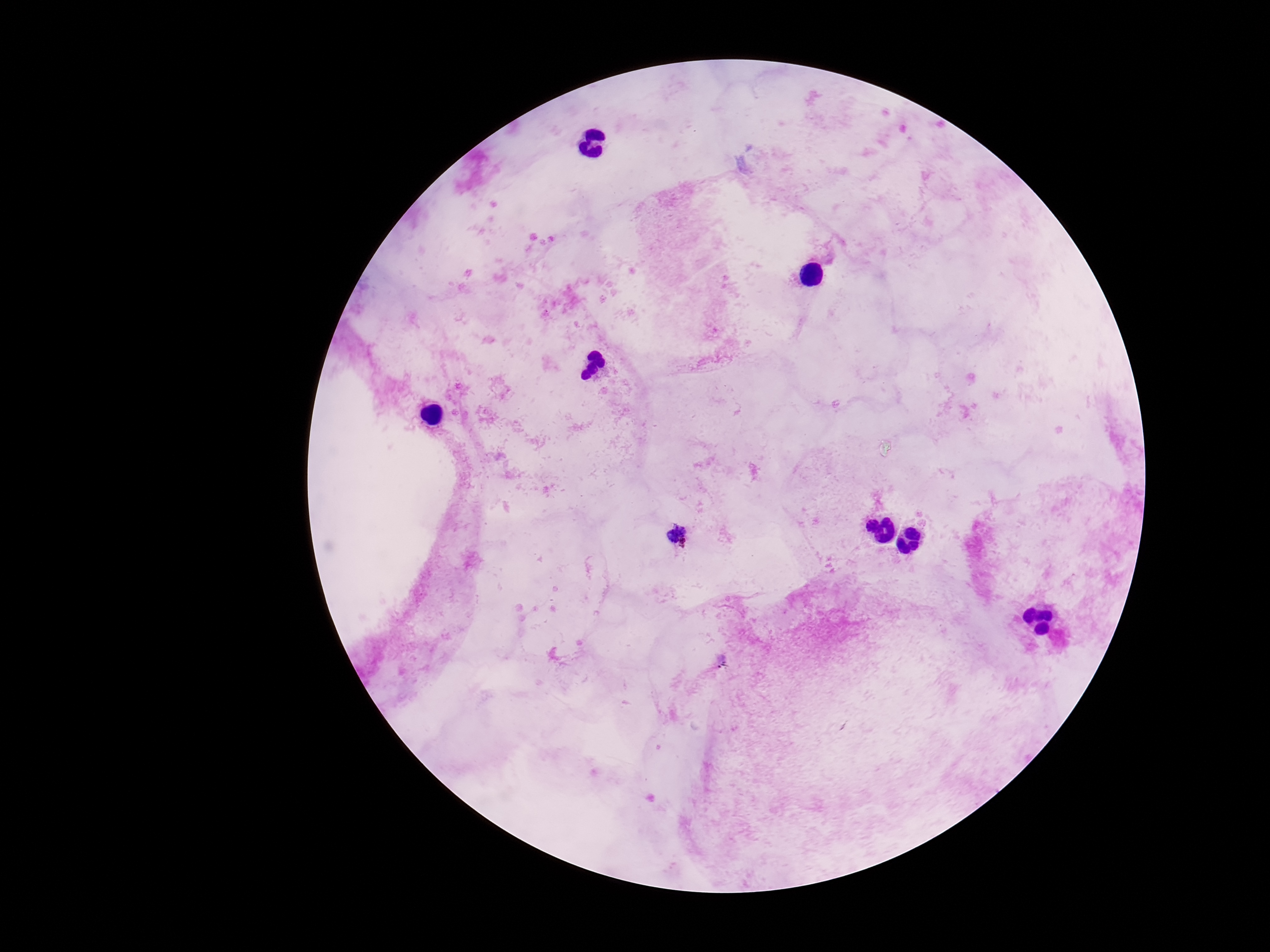
patient malaria status = infected
magnification = 100x
preparation = thick blood film
Plasmodium parasite locations = approximate centers as {x, y} in pixels: {678, 536}
capture = smartphone camera through the microscope eyepiece
image size = 1270×952 pixels
stain = Giemsa
field of view = single